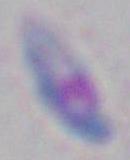

Summary:
  - Modality: micrograph
  - Magnification: 1000x
  - Identification: Toxoplasma gondii